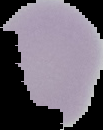 Malaria status: uninfected. Image is 103×130 pixels. The area outside the segmented cell region is set to black. From a thin blood film.